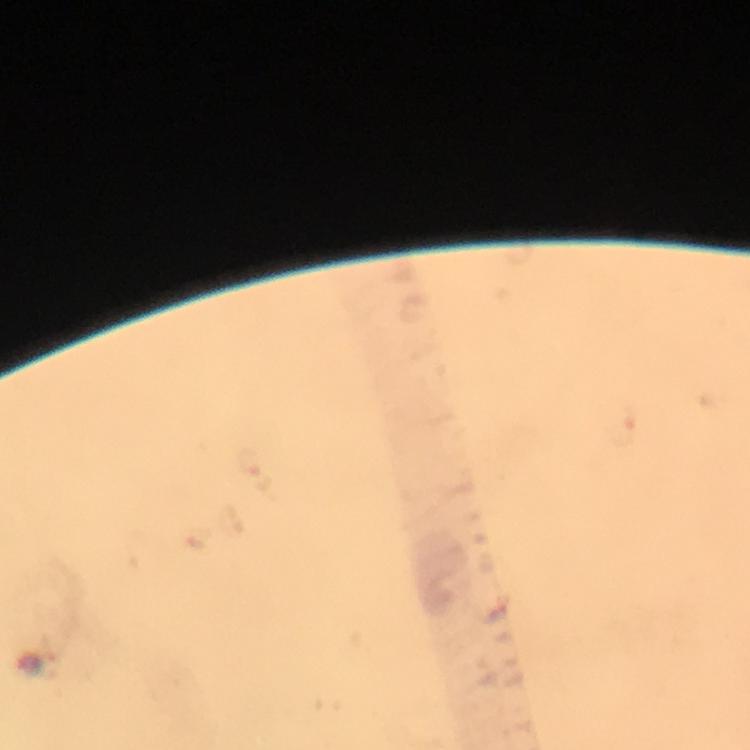

{
  "cropped_from": "a single field of view",
  "capture": "smartphone mounted on the microscope",
  "malaria_parasite_locations": "approximate centers as {x, y} in pixels: {38, 663}",
  "preparation": "thick smear",
  "context": "from a malaria diagnostic workup",
  "stain": "Giemsa",
  "magnification": "100x",
  "immersion_oil": "used",
  "image_size": "750×750 pixels"
}